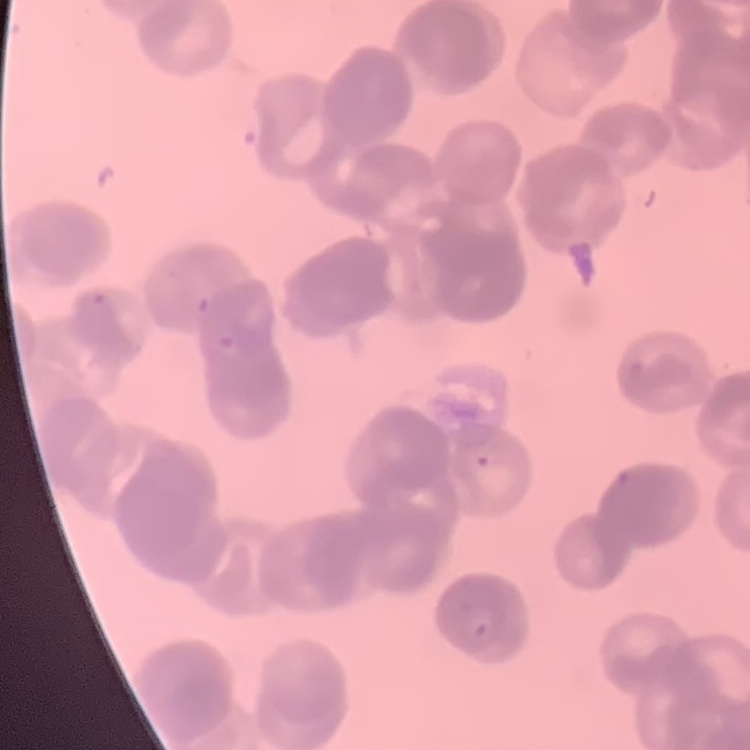

{
  "erythrocyte_morphology": "rouleaux formation",
  "image_type": "square crop of a larger photomicrograph",
  "preparation": "thin blood film",
  "stain": "Field's or Giemsa"
}